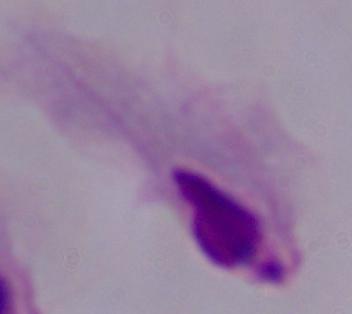
Summary:
  - Magnification: 1000x
  - Identification: trichomonad
  - Modality: micrograph